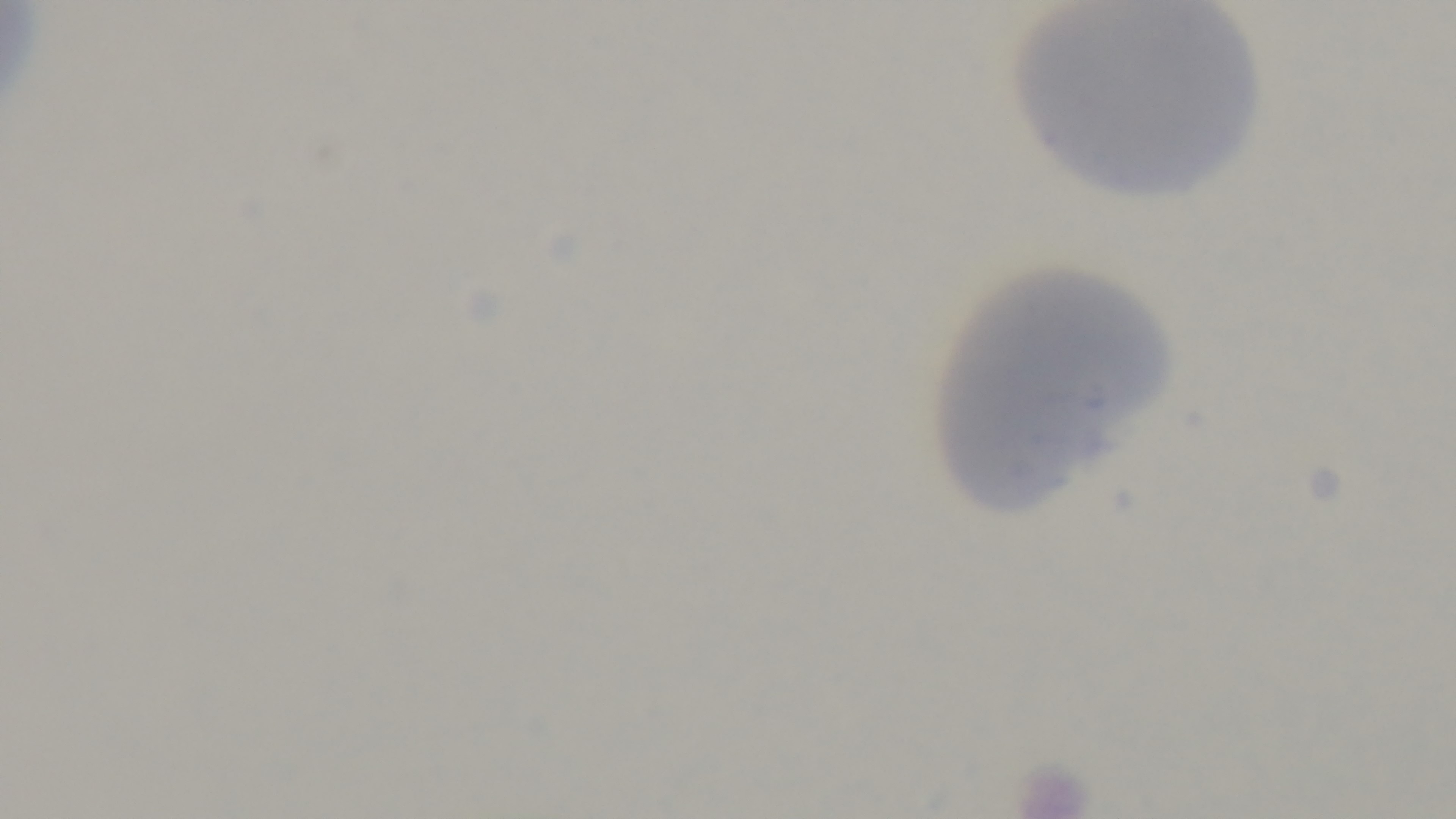
stain: Giemsa
preparation: thin smear
modality: light microscopy
field_of_view: single
malaria_status: uninfected
capture: mounted 4K digital camera
objective: 100x oil immersion